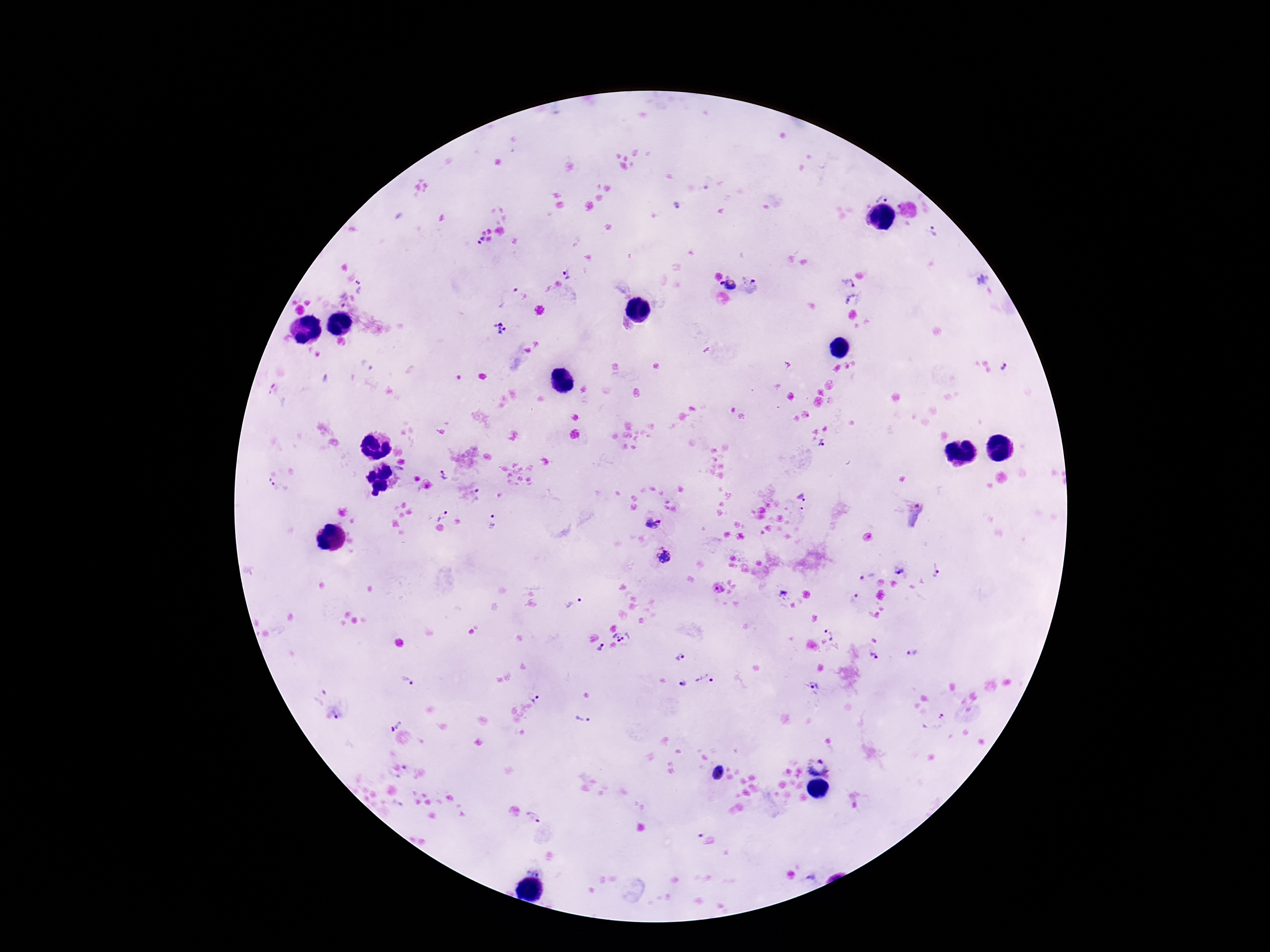

Approximate object centers, in pixels from the top-left corner. Plasmodium parasite locations: (x=882, y=194), (x=678, y=205), (x=933, y=233), (x=477, y=241), (x=569, y=271), (x=982, y=279), (x=848, y=281), (x=729, y=283), (x=360, y=286), (x=752, y=286), (x=503, y=294), (x=342, y=298), (x=853, y=300), (x=501, y=326), (x=368, y=365), (x=1005, y=368), (x=823, y=445), (x=445, y=475), (x=279, y=489), (x=481, y=494), (x=802, y=497), (x=441, y=515), (x=918, y=515), (x=492, y=522), (x=655, y=524), (x=663, y=555), (x=935, y=570), (x=899, y=571), (x=867, y=575), (x=718, y=588), (x=784, y=592), (x=855, y=598), (x=574, y=604), (x=831, y=631), (x=624, y=635), (x=601, y=649), (x=912, y=654), (x=681, y=656), (x=875, y=656), (x=406, y=679), (x=707, y=679), (x=682, y=683), (x=814, y=687), (x=536, y=695), (x=336, y=715), (x=583, y=718), (x=941, y=719), (x=393, y=725), (x=817, y=765), (x=718, y=774), (x=534, y=817), (x=702, y=833), (x=813, y=877). Image is 1270×952 pixels. Giemsa stain. Single field of view. 100x magnification. Thick peripheral-blood smear. Photographed through the microscope eyepiece with a smartphone camera. Patient malaria status: positive.